Outline each uninfected red blood cell.
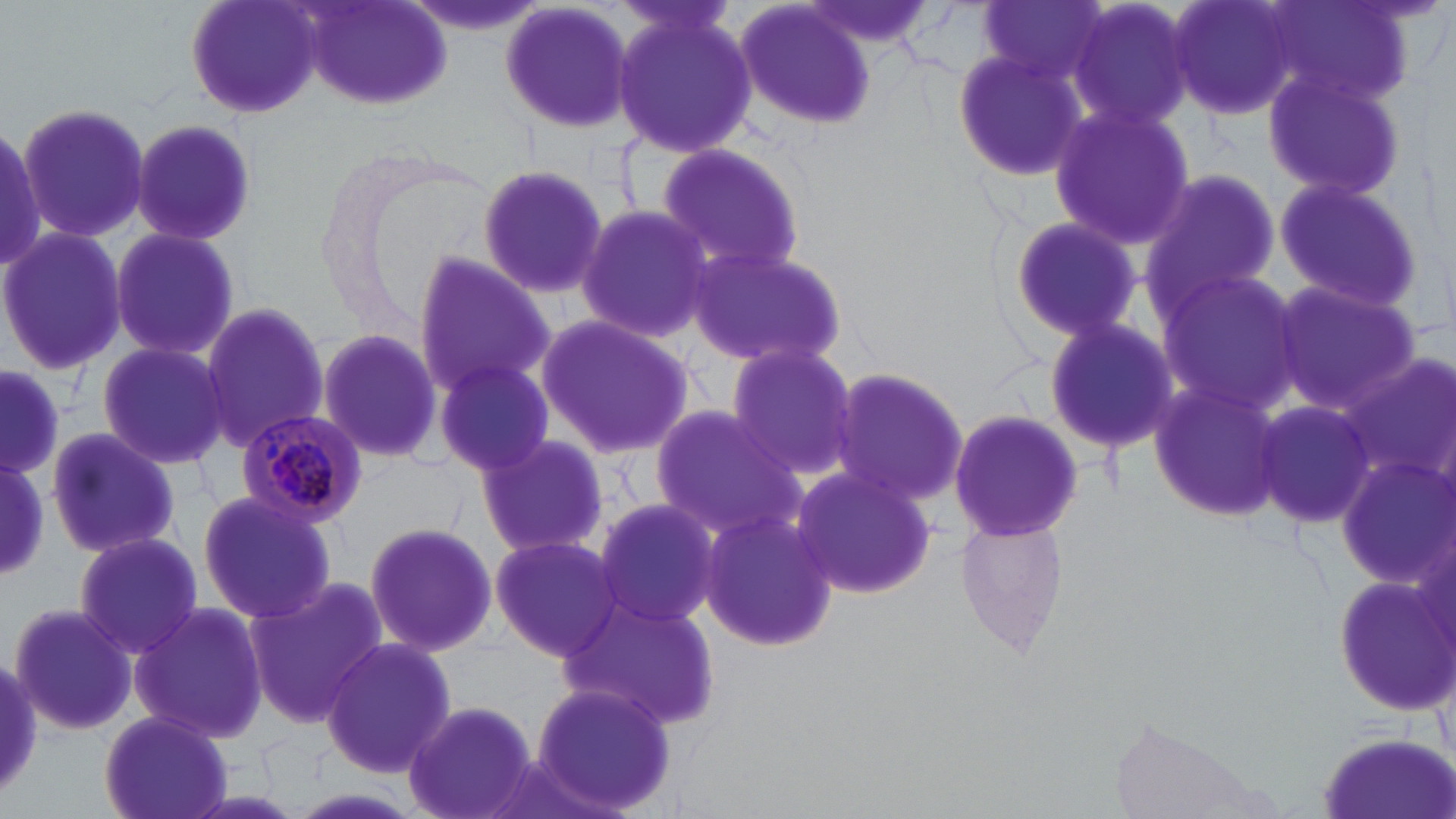
Approximate bounding boxes as (x1,y1)-(x2,y2) corner pairs in pixels.
Uninfected red blood cells: (182,0)-(326,118), (299,0)-(455,111), (733,0)-(879,133), (804,0)-(934,55), (1064,0)-(1201,136), (1168,0)-(1306,124), (1265,0)-(1419,112), (499,1)-(638,137), (612,2)-(758,163), (975,2)-(1112,88), (950,49)-(1086,183), (1262,65)-(1408,204), (17,101)-(151,247), (1047,102)-(1195,251), (127,118)-(259,246), (0,122)-(46,276), (655,142)-(809,281), (475,162)-(612,301), (1141,168)-(1282,308), (1272,176)-(1425,313), (575,206)-(716,344), (1005,214)-(1143,343), (0,227)-(125,375), (107,227)-(239,363), (681,243)-(848,370), (411,253)-(553,397), (1152,269)-(1301,414), (1271,282)-(1422,418), (198,301)-(329,453), (533,310)-(697,460), (1041,315)-(1183,454), (315,325)-(449,467), (96,339)-(231,469), (723,342)-(860,480), (1336,354)-(1456,491), (435,358)-(556,476), (831,364)-(971,512), (0,368)-(65,475), (1145,380)-(1287,525), (1254,398)-(1379,531), (649,406)-(803,538), (948,407)-(1087,541), (43,425)-(183,560), (474,434)-(610,560), (1335,455)-(1454,592), (0,458)-(48,576), (789,465)-(940,598), (194,488)-(339,625), (590,496)-(725,631), (697,506)-(840,653), (956,512)-(1068,656), (360,518)-(499,655), (70,532)-(205,658), (487,533)-(628,662), (1328,570)-(1456,715), (244,577)-(387,727), (556,595)-(724,733), (129,600)-(269,746), (7,601)-(138,736), (320,637)-(456,778), (0,659)-(43,798), (531,680)-(678,817), (401,699)-(537,819), (98,712)-(231,819), (1317,731)-(1455,819), (474,751)-(605,819), (284,787)-(429,819).

Summary:
  - Plasmodium malariae-infected red blood cell locations: (235,409)-(367,527)
  - Slide-level diagnosis: Plasmodium malariae
  - Field of view: single
  - Preparation: thin blood film
  - Image size: 1456×819 pixels
  - Magnification: 1000x
  - Modality: optical microscopy
  - Stain: May-Grünwald-Giemsa